Locate and identify every blood parasite.
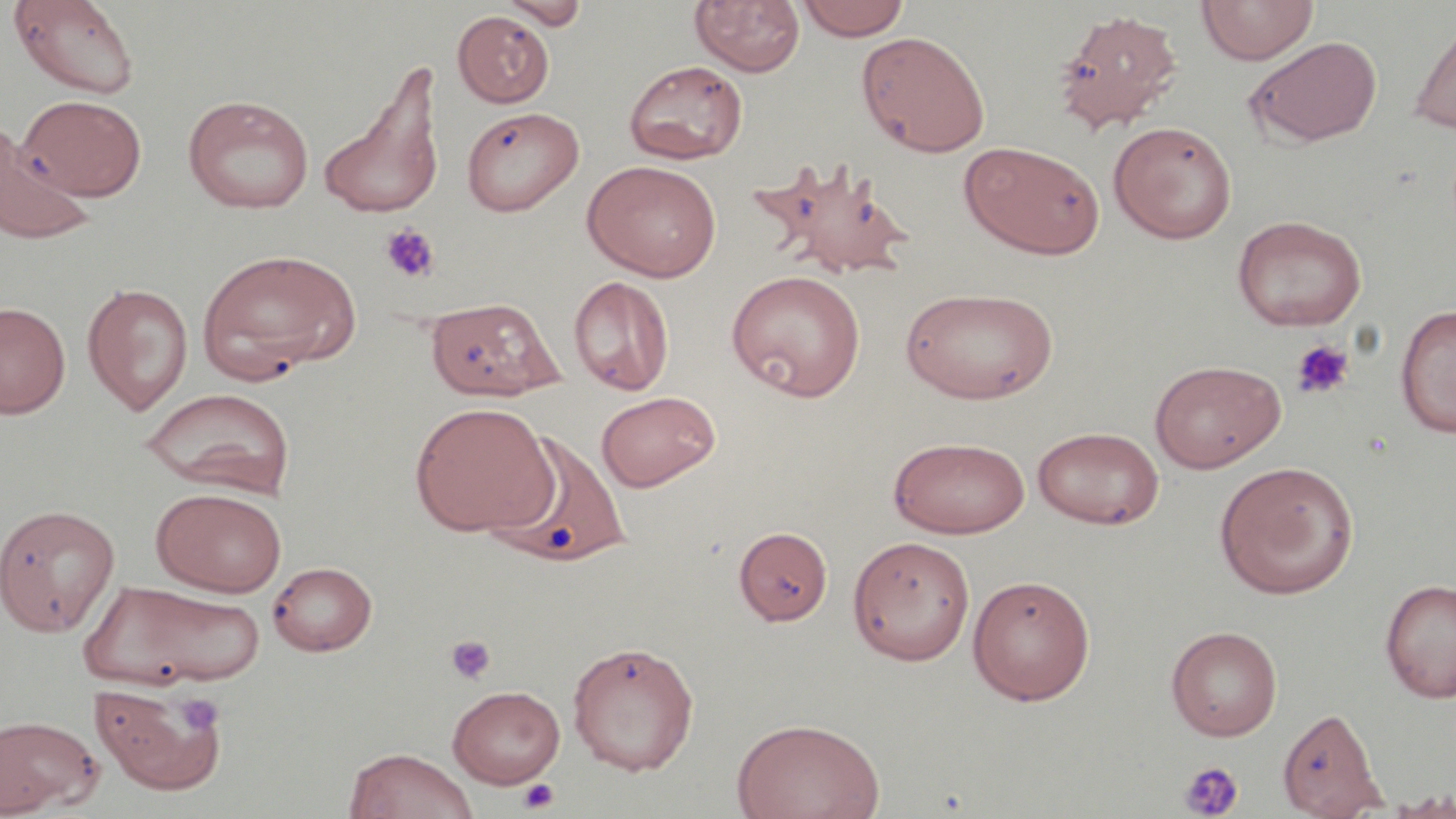
No blood parasites seen.

slide-level diagnosis = negative for blood parasites
image size = 1456×819 pixels
preparation = thin blood film
platelet locations = approximate bounding boxes as named x1/y1/x2/y2 corners in pixels: (x1=381, y1=223, x2=441, y2=284), (x1=1290, y1=339, x2=1355, y2=400), (x1=445, y1=635, x2=497, y2=685), (x1=177, y1=694, x2=224, y2=734), (x1=1178, y1=760, x2=1245, y2=818), (x1=516, y1=778, x2=560, y2=814)
stain = May-Grünwald-Giemsa
field of view = one of a larger specimen
uninfected red blood cell locations = approximate bounding boxes as named x1/y1/x2/y2 corners in pixels: (x1=7, y1=0, x2=141, y2=99), (x1=499, y1=0, x2=589, y2=29), (x1=690, y1=0, x2=805, y2=77), (x1=795, y1=0, x2=912, y2=41), (x1=1196, y1=0, x2=1319, y2=66), (x1=1052, y1=9, x2=1184, y2=135), (x1=452, y1=10, x2=554, y2=108), (x1=1409, y1=16, x2=1456, y2=136), (x1=857, y1=31, x2=991, y2=158), (x1=1243, y1=36, x2=1382, y2=147), (x1=624, y1=59, x2=748, y2=165), (x1=320, y1=71, x2=444, y2=219), (x1=183, y1=94, x2=314, y2=213), (x1=20, y1=95, x2=146, y2=200), (x1=460, y1=105, x2=585, y2=217), (x1=1108, y1=120, x2=1237, y2=243), (x1=0, y1=127, x2=94, y2=245), (x1=960, y1=141, x2=1105, y2=259), (x1=755, y1=159, x2=919, y2=281), (x1=582, y1=160, x2=722, y2=281), (x1=1231, y1=214, x2=1367, y2=330), (x1=197, y1=248, x2=359, y2=380), (x1=726, y1=269, x2=866, y2=400), (x1=568, y1=276, x2=675, y2=396), (x1=82, y1=283, x2=194, y2=415), (x1=899, y1=286, x2=1059, y2=405), (x1=424, y1=296, x2=562, y2=401), (x1=0, y1=301, x2=71, y2=418), (x1=1395, y1=304, x2=1456, y2=437), (x1=1149, y1=359, x2=1286, y2=472), (x1=141, y1=386, x2=295, y2=499), (x1=596, y1=390, x2=721, y2=493), (x1=409, y1=402, x2=556, y2=536), (x1=1032, y1=426, x2=1165, y2=530), (x1=484, y1=430, x2=632, y2=568), (x1=888, y1=436, x2=1030, y2=539), (x1=1214, y1=461, x2=1359, y2=599), (x1=151, y1=487, x2=287, y2=597), (x1=0, y1=503, x2=120, y2=637), (x1=733, y1=527, x2=833, y2=625), (x1=847, y1=535, x2=976, y2=665), (x1=267, y1=560, x2=378, y2=656), (x1=967, y1=573, x2=1096, y2=705), (x1=1380, y1=578, x2=1456, y2=703), (x1=81, y1=579, x2=266, y2=690), (x1=1166, y1=625, x2=1283, y2=740), (x1=567, y1=641, x2=700, y2=775), (x1=88, y1=680, x2=228, y2=796), (x1=447, y1=685, x2=565, y2=788), (x1=1277, y1=706, x2=1387, y2=818), (x1=0, y1=714, x2=103, y2=816), (x1=731, y1=717, x2=886, y2=819), (x1=343, y1=747, x2=479, y2=819), (x1=1383, y1=791, x2=1456, y2=818)
modality = light microscopy
magnification = 1000x